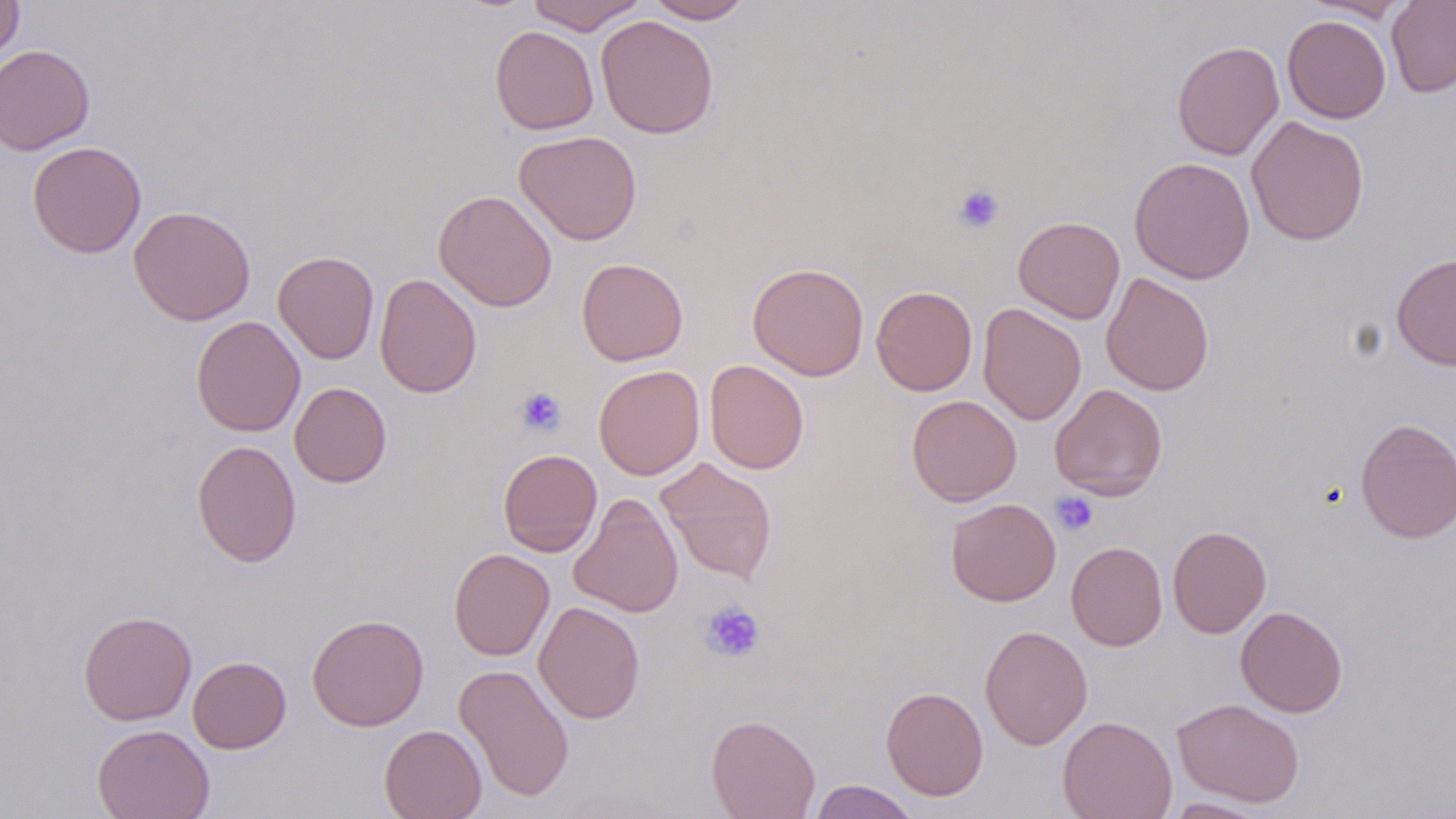
slide-level diagnosis = no evidence of blood parasites
stain = May-Grünwald-Giemsa
uninfected red blood cell locations = approximate bounding boxes as [x1, y1, x2, y2] in pixels: [0, 0, 24, 69], [527, 0, 647, 34], [644, 0, 754, 23], [1302, 0, 1410, 22], [1386, 1, 1456, 98], [595, 15, 719, 139], [1282, 15, 1391, 123], [490, 25, 599, 134], [1171, 40, 1284, 161], [0, 44, 95, 155], [1246, 116, 1369, 246], [514, 130, 642, 245], [27, 141, 147, 258], [1129, 156, 1255, 284], [433, 189, 557, 312], [128, 205, 255, 325], [1014, 216, 1125, 324], [273, 250, 379, 364], [1391, 252, 1456, 370], [576, 258, 688, 366], [748, 262, 869, 380], [374, 273, 482, 398], [1101, 273, 1214, 396], [871, 286, 977, 396], [978, 302, 1086, 425], [191, 315, 306, 437], [704, 359, 809, 474], [593, 364, 704, 480], [289, 382, 391, 487], [1050, 383, 1167, 500], [906, 395, 1022, 506], [1354, 416, 1456, 543], [191, 439, 302, 567], [497, 449, 602, 556], [655, 457, 778, 584], [568, 493, 684, 618], [946, 498, 1061, 606], [1167, 525, 1271, 638], [1066, 541, 1167, 651], [449, 548, 555, 661], [533, 601, 646, 724], [1235, 606, 1348, 717], [78, 610, 197, 725], [306, 613, 429, 731], [979, 624, 1092, 750], [188, 656, 291, 754], [453, 663, 574, 803], [881, 686, 989, 800], [1172, 698, 1304, 807], [706, 714, 820, 819], [1057, 715, 1177, 819], [92, 724, 215, 819], [379, 724, 487, 819], [808, 780, 922, 818], [1161, 798, 1272, 818]
image size = 1456×819 pixels
platelet locations = approximate bounding boxes as [x1, y1, x2, y2] in pixels: [952, 183, 1005, 234], [516, 387, 566, 436], [1050, 491, 1098, 536], [698, 601, 764, 663]
preparation = thin blood smear
field of view = one of a larger specimen
magnification = 1000x
modality = optical microscopy